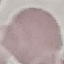
result = no malaria parasites detected
stain = Giemsa
image type = automatically extracted cell patch, resized to 64 × 64 pixels
capture = smartphone through the microscope eyepiece
preparation = thin smear